State which parasite is depicted.
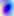

Toxoplasma gondii.

Photomicrograph. 400x magnification.